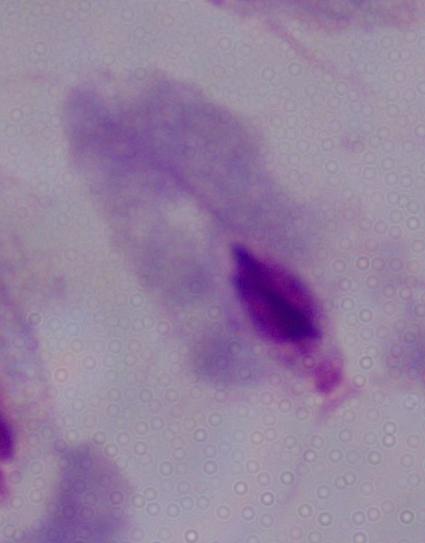 Micrograph. A trichomonad is seen. Captured at 1000x magnification.